Identify the parasite.
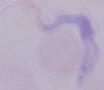
A trypanosome.

modality = micrograph
magnification = 1000x